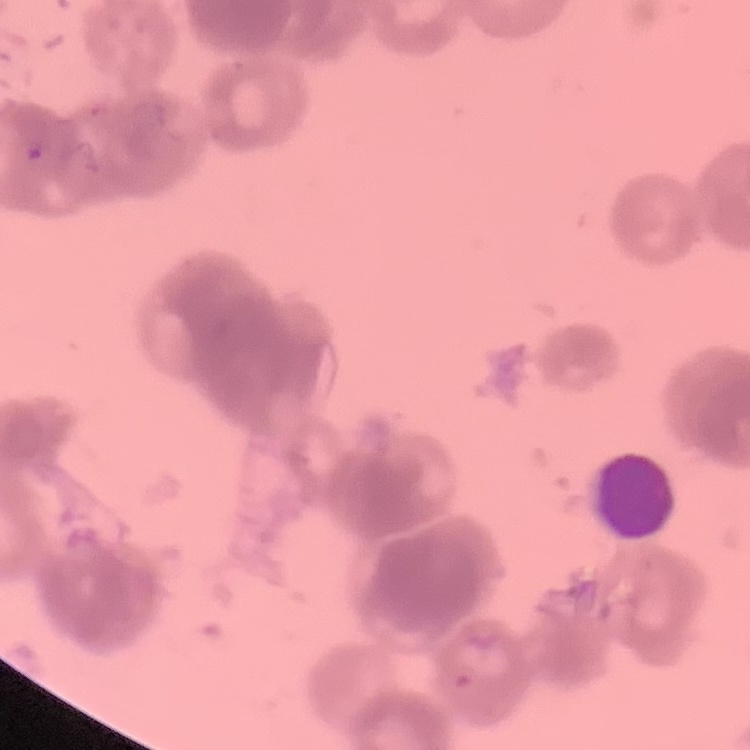 The red blood cells exhibit rouleaux formation. Square crop of a larger photomicrograph. Thin blood smear. Field's or Giemsa stain.